Locate and identify every blood parasite.
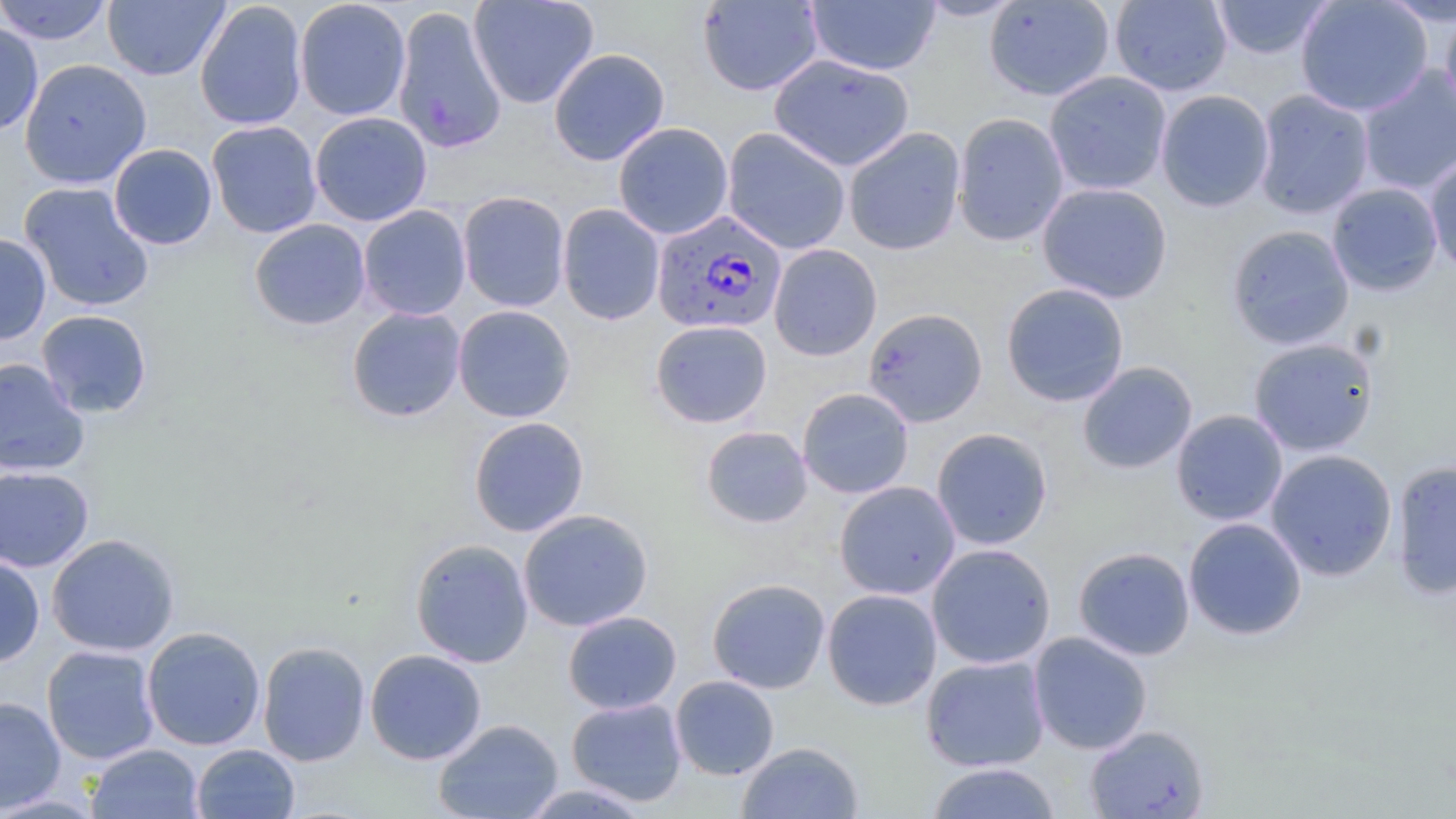
Approximate bounding boxes as (x1, y1, x2, y2) in pixels.
Plasmodium falciparum-infected red blood cells: (652, 212, 793, 335).
No Plasmodium ovale, Plasmodium malariae, Plasmodium vivax, Babesia divergens, or Trypanosoma brucei observed.

Uninfected red blood cell locations: (0, 0, 113, 45), (103, 0, 229, 81), (294, 0, 412, 121), (467, 0, 599, 109), (916, 0, 1025, 21), (983, 0, 1116, 101), (1109, 0, 1232, 96), (1209, 0, 1334, 60), (1295, 0, 1433, 117), (1379, 0, 1456, 26), (194, 1, 308, 131), (696, 1, 824, 96), (805, 1, 941, 75), (392, 5, 507, 155), (1440, 9, 1456, 121), (0, 22, 44, 135), (548, 48, 670, 166), (769, 53, 914, 171), (19, 58, 151, 188), (1357, 65, 1456, 196), (1044, 71, 1172, 196), (1156, 89, 1275, 212), (1253, 89, 1375, 219), (310, 111, 432, 226), (952, 112, 1069, 246), (206, 120, 322, 238), (612, 122, 734, 239), (722, 127, 851, 255), (843, 127, 966, 256), (109, 143, 217, 250), (1424, 152, 1456, 279), (19, 181, 155, 312), (1037, 181, 1173, 304), (1326, 182, 1443, 297), (457, 191, 570, 312), (557, 204, 665, 325), (358, 205, 472, 321), (249, 219, 371, 330), (1226, 224, 1355, 350), (0, 233, 51, 344), (769, 244, 882, 360), (1000, 283, 1130, 406), (452, 304, 576, 423), (346, 306, 466, 423), (863, 307, 988, 426), (36, 309, 153, 418), (650, 319, 772, 428), (1248, 337, 1379, 457), (0, 358, 90, 477), (1077, 361, 1197, 474), (797, 387, 914, 499), (1171, 409, 1288, 526), (468, 416, 589, 537), (701, 425, 813, 528), (931, 427, 1053, 550), (1265, 449, 1398, 580), (1390, 460, 1456, 599), (0, 465, 94, 572), (834, 481, 961, 600), (518, 509, 654, 632), (1183, 517, 1307, 640), (46, 533, 180, 657), (410, 538, 534, 668), (926, 543, 1056, 669), (1072, 546, 1195, 660), (0, 555, 46, 667), (706, 577, 831, 694), (822, 588, 942, 710), (563, 610, 682, 714), (141, 626, 266, 750), (1029, 632, 1153, 754), (257, 641, 370, 767), (41, 645, 160, 764), (365, 648, 487, 765), (921, 654, 1050, 772), (670, 675, 779, 780), (0, 696, 66, 815), (566, 697, 687, 807), (433, 718, 563, 819), (1085, 724, 1210, 818), (736, 741, 864, 819), (86, 743, 204, 818), (192, 743, 299, 819), (925, 761, 1062, 819), (517, 783, 655, 818). Slide-level diagnosis: Plasmodium falciparum. Captured at 1000x magnification. Light microscopy. May-Grünwald-Giemsa stain. One field of a larger specimen. Thin blood film. Image is 1456×819 pixels.